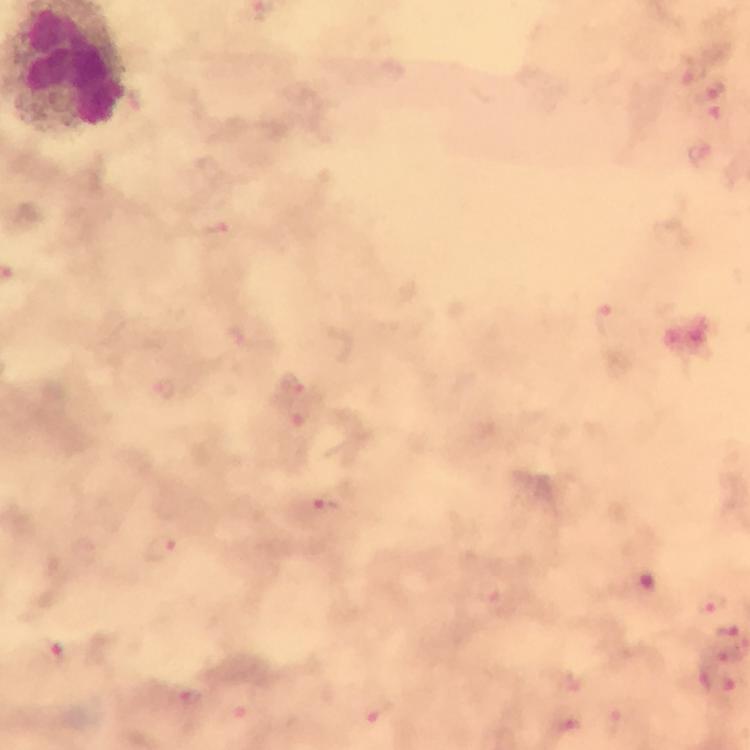 Approximate centers as (x, y) in pixels. Plasmodium parasite locations: (716, 91), (699, 157), (215, 233), (606, 319), (293, 381), (324, 504), (161, 548), (712, 605), (725, 631), (54, 650), (719, 681), (384, 713), (569, 730). Image is 750×750 pixels. At 100x magnification. A crop from one field of view. Immersion oil was used. From a malaria diagnostic workup. Photographed through the microscope with a smartphone camera. Thick smear. Giemsa stain.